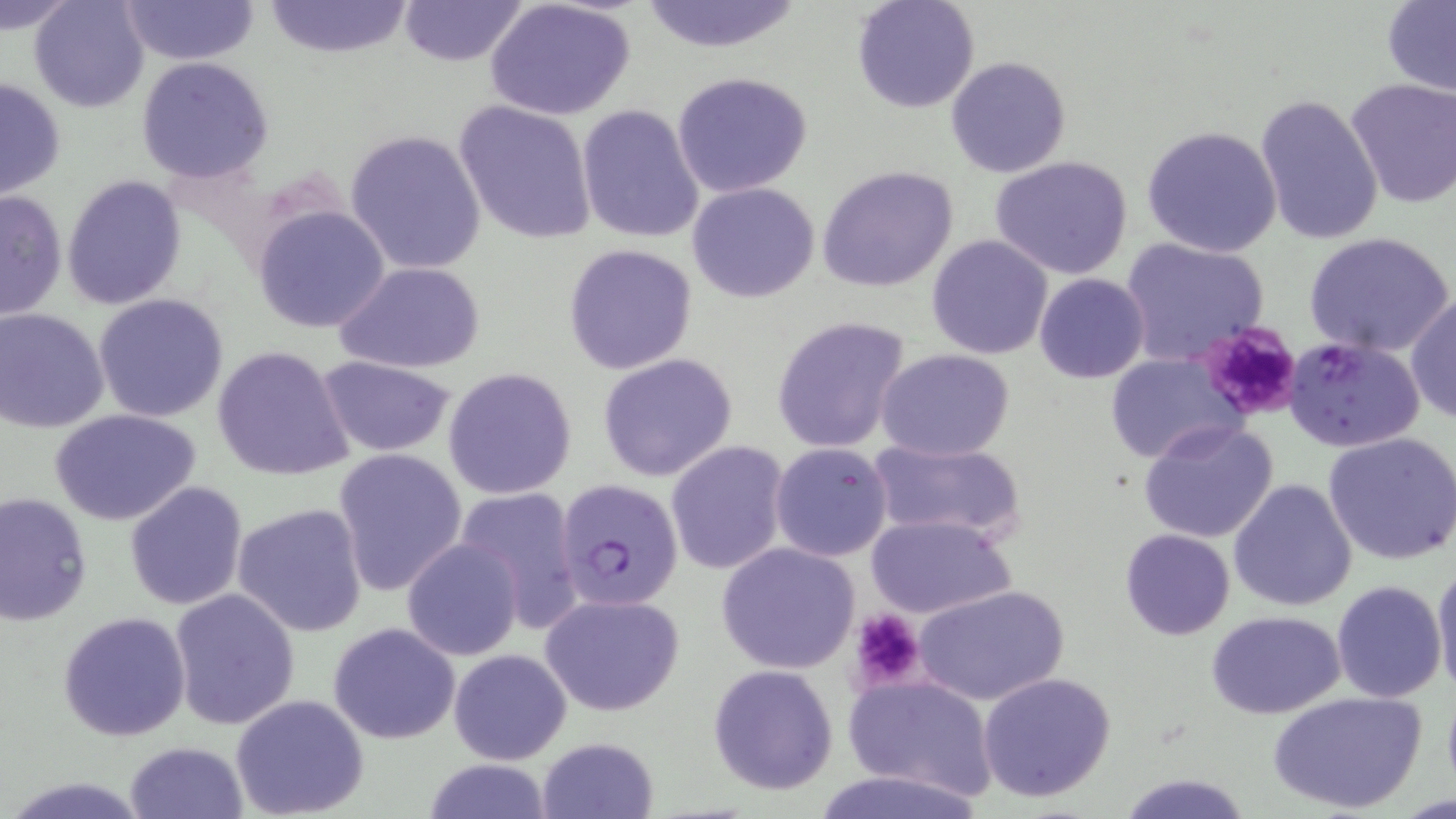
Summary:
  - Coordinate format: approximate bounding boxes as (x1, y1, x2, y2) in pixels
  - Platelet locations: (1198, 319, 1305, 421), (849, 608, 926, 691)
  - Plasmodium falciparum-infected red blood cell locations: (1285, 337, 1426, 455), (555, 478, 683, 610)
  - Uninfected red blood cell locations: (0, 0, 80, 34), (29, 0, 150, 113), (120, 0, 259, 66), (260, 0, 413, 57), (396, 0, 529, 67), (637, 0, 803, 53), (851, 0, 980, 115), (485, 1, 636, 121), (1379, 2, 1456, 96), (136, 56, 273, 184), (945, 56, 1071, 178), (671, 71, 813, 198), (1, 77, 68, 200), (1342, 78, 1456, 210), (1254, 92, 1384, 246), (452, 99, 598, 245), (576, 105, 706, 245), (1141, 123, 1284, 258), (344, 129, 487, 275), (990, 155, 1135, 280), (817, 165, 959, 293), (62, 175, 187, 310), (686, 181, 820, 302), (0, 188, 66, 321), (253, 206, 390, 333), (1304, 232, 1455, 358), (927, 235, 1054, 358), (1118, 236, 1270, 368), (563, 242, 697, 375), (336, 260, 485, 375), (1034, 273, 1150, 383), (93, 294, 229, 425), (1406, 296, 1455, 423), (0, 309, 109, 432), (770, 315, 912, 454), (210, 345, 353, 484), (876, 349, 1015, 461), (595, 352, 738, 482), (1103, 352, 1244, 463), (316, 357, 457, 455), (444, 368, 578, 501), (50, 408, 201, 526), (1138, 418, 1282, 543), (1324, 430, 1456, 564), (866, 439, 1028, 543), (666, 440, 789, 577), (770, 443, 893, 562), (331, 449, 468, 597), (1229, 478, 1358, 611), (124, 481, 249, 611), (453, 486, 585, 630), (1, 491, 93, 625), (232, 502, 369, 637), (864, 513, 1015, 620), (1120, 528, 1235, 640), (402, 538, 522, 662), (717, 543, 859, 673), (1433, 561, 1456, 697), (1332, 580, 1447, 702), (913, 584, 1070, 707), (168, 587, 301, 729), (538, 591, 684, 716), (1206, 609, 1345, 719), (58, 610, 191, 742), (328, 621, 461, 743), (447, 648, 572, 764), (708, 664, 839, 795), (975, 672, 1118, 803), (844, 675, 996, 799), (1267, 689, 1428, 814), (228, 693, 370, 819), (536, 736, 660, 819), (124, 740, 250, 819), (417, 758, 558, 818), (806, 767, 990, 819), (1118, 772, 1253, 818)
  - Slide-level diagnosis: Plasmodium falciparum
  - Preparation: thin blood film
  - Field of view: one of a larger specimen
  - Modality: optical microscopy
  - Image size: 1456×819 pixels
  - Magnification: 1000x
  - Stain: May-Grünwald-Giemsa